Report the malaria status of this cell.
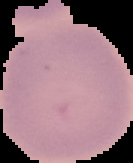
Uninfected.

From a thin blood smear. Segmented cell region on a black background. Image is 133×163 pixels.